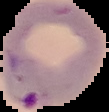
Summary:
  - Image type: segmented cell region with the area outside set to black
  - Result: Plasmodium parasites identified
  - Preparation: thin blood film
  - Image size: 109×112 pixels